Outline each Plasmodium falciparum-infected red blood cell.
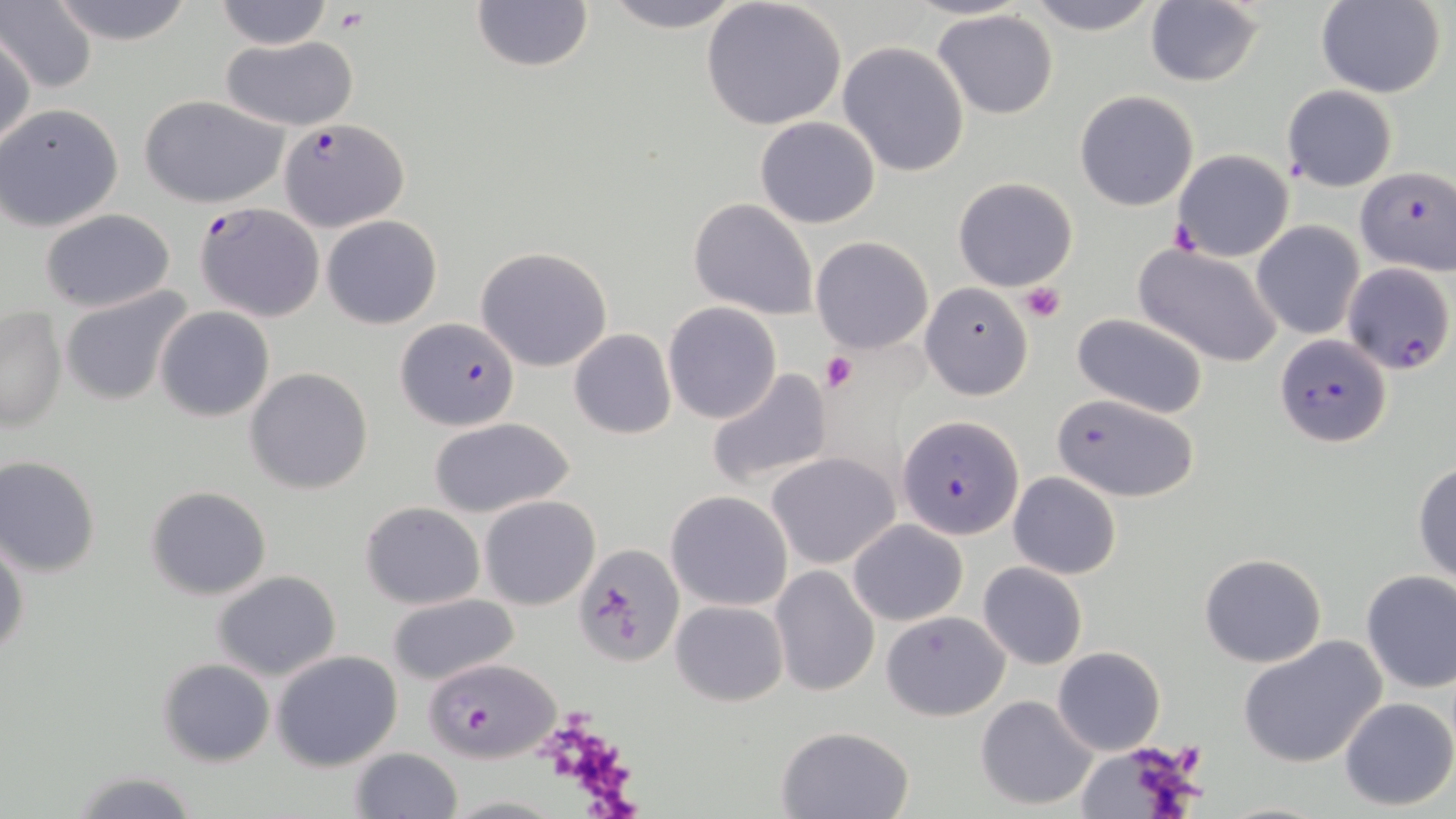

Approximate bounding boxes as (x1, y1, x2, y2) in pixels.
Plasmodium falciparum-infected red blood cells: (280, 118, 410, 232), (1356, 167, 1455, 275), (198, 201, 326, 321), (397, 318, 520, 430), (1275, 334, 1390, 447), (1049, 391, 1195, 502), (897, 415, 1024, 539), (423, 658, 558, 762).

Platelet locations: (334, 8, 365, 34), (1019, 281, 1065, 324), (821, 349, 858, 392). Uninfected red blood cell locations: (48, 0, 195, 45), (213, 0, 333, 49), (597, 0, 752, 32), (1021, 0, 1166, 37), (3, 1, 99, 93), (470, 1, 595, 74), (700, 1, 849, 134), (1316, 1, 1445, 97), (1145, 2, 1263, 87), (932, 10, 1058, 119), (1, 29, 34, 151), (217, 35, 363, 130), (837, 42, 970, 177), (1281, 86, 1397, 192), (1075, 91, 1200, 211), (138, 93, 290, 208), (0, 102, 124, 231), (755, 116, 881, 230), (768, 142, 912, 288), (1170, 149, 1294, 262), (953, 176, 1079, 292), (688, 197, 819, 319), (38, 208, 177, 312), (322, 215, 442, 329), (1252, 221, 1364, 340), (810, 237, 934, 354), (1134, 242, 1285, 368), (476, 246, 614, 372), (1342, 261, 1455, 375), (920, 283, 1034, 400), (59, 285, 195, 408), (663, 302, 782, 424), (1, 306, 68, 434), (155, 306, 274, 422), (1070, 313, 1210, 419), (569, 329, 676, 440), (710, 365, 834, 493), (245, 367, 374, 495), (427, 417, 574, 518), (765, 452, 900, 570), (0, 457, 102, 577), (1413, 461, 1456, 586), (1007, 472, 1121, 580), (144, 486, 272, 600), (666, 490, 792, 611), (480, 495, 600, 609), (360, 502, 484, 608), (848, 520, 968, 627), (0, 532, 28, 664), (574, 544, 684, 665), (1198, 552, 1328, 667), (978, 561, 1087, 670), (771, 566, 879, 696), (1360, 570, 1456, 693), (211, 571, 342, 682), (388, 594, 519, 687), (672, 599, 788, 706), (881, 611, 1010, 720), (1239, 635, 1387, 768), (1053, 647, 1166, 755), (270, 649, 403, 771), (157, 658, 274, 767), (976, 694, 1099, 812), (1338, 697, 1455, 810), (775, 724, 917, 818), (1080, 742, 1204, 819), (349, 747, 465, 819), (68, 769, 201, 818). Slide-level diagnosis: Plasmodium falciparum. Light microscopy. One field of a larger specimen. May-Grünwald-Giemsa-stained preparation. Thin blood film. Image is 1456×819 pixels. Captured at 1000x magnification.